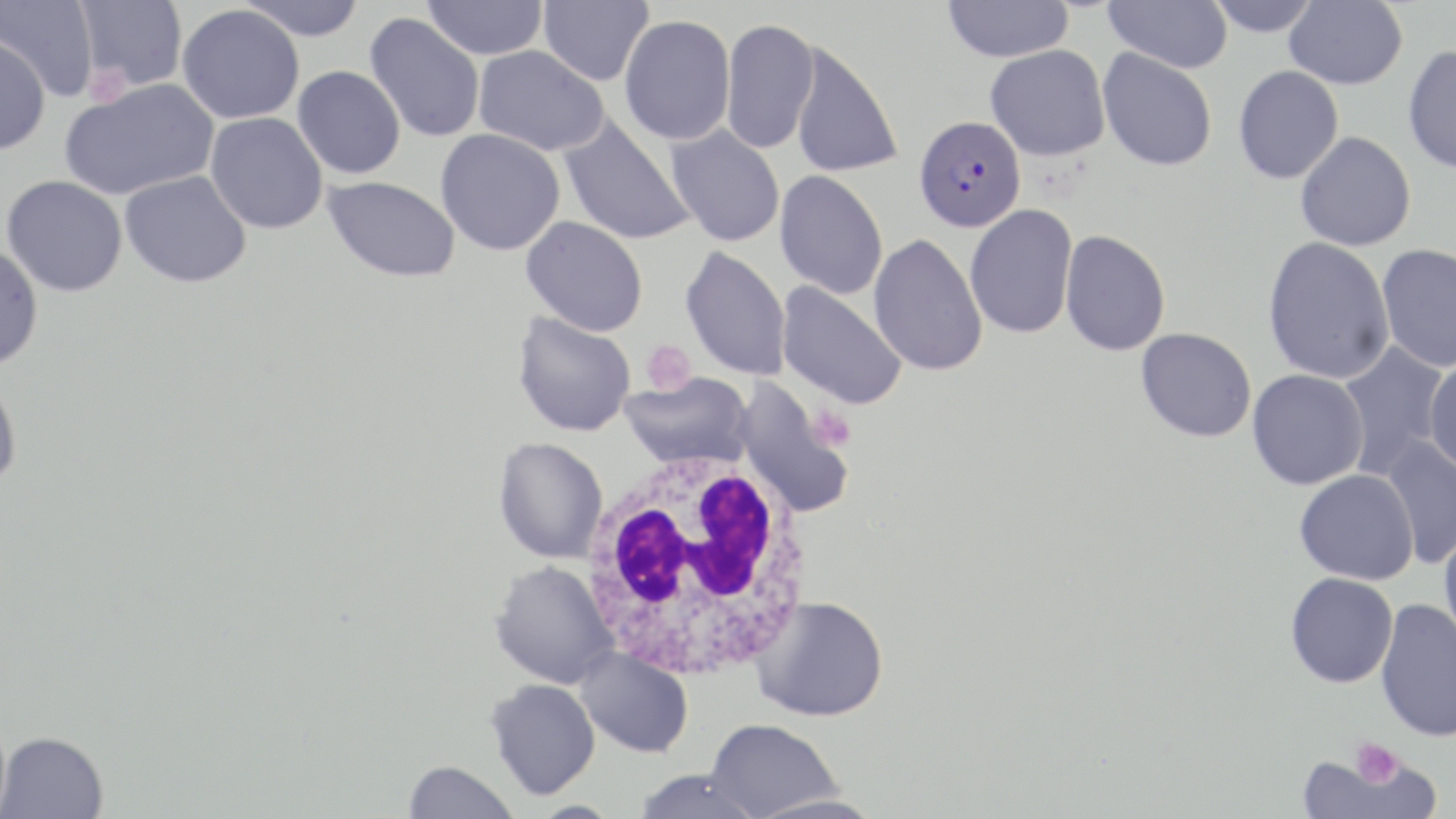

slide-level diagnosis = Plasmodium falciparum
preparation = thin blood film
magnification = 1000x
modality = light microscopy
platelet locations = approximate bounding boxes as (x1,y1)-(x2,y2) corner pairs in pixels: (82,67)-(130,108), (640,339)-(697,395), (808,404)-(855,451), (1349,737)-(1402,788)
uninfected red blood cell locations = approximate bounding boxes as (x1,y1)-(x2,y2) corner pairs in pixels: (0,0)-(100,102), (75,0)-(187,91), (235,0)-(367,41), (422,0)-(548,60), (538,0)-(653,86), (941,0)-(1074,63), (1104,0)-(1232,73), (1205,0)-(1322,37), (1284,1)-(1408,90), (177,5)-(304,124), (365,13)-(485,143), (619,15)-(736,145), (721,18)-(821,155), (0,35)-(50,156), (790,41)-(903,179), (1403,44)-(1456,174), (473,45)-(609,156), (985,45)-(1110,161), (1097,47)-(1218,171), (293,65)-(406,179), (1232,66)-(1343,185), (60,79)-(220,200), (557,112)-(697,247), (205,113)-(328,234), (665,123)-(786,248), (435,129)-(566,256), (1295,131)-(1416,251), (119,170)-(252,289), (775,170)-(888,300), (2,176)-(128,297), (322,176)-(461,283), (964,204)-(1078,339), (521,216)-(649,336), (1060,229)-(1170,357), (869,233)-(988,377), (1262,236)-(1396,385), (1376,243)-(1456,372), (0,244)-(44,370), (680,245)-(792,381), (776,281)-(908,410), (512,312)-(636,437), (1135,327)-(1257,443), (1336,341)-(1450,479), (1424,355)-(1456,479), (1247,369)-(1369,490), (621,372)-(754,471), (0,373)-(23,491), (734,379)-(855,517), (1380,435)-(1456,570), (492,436)-(608,564), (1294,469)-(1419,585), (1438,527)-(1456,647), (487,560)-(619,689), (1285,573)-(1398,688), (751,596)-(889,722), (1375,599)-(1456,743), (574,647)-(694,758), (485,679)-(601,801), (705,718)-(843,819), (0,731)-(108,819), (1298,750)-(1426,819), (402,760)-(519,819), (632,769)-(763,819), (748,792)-(883,819)
Plasmodium falciparum-infected red blood cell locations = approximate bounding boxes as (x1,y1)-(x2,y2) corner pairs in pixels: (914,115)-(1026,232)
image size = 1456×819 pixels
white blood cell locations = approximate bounding boxes as (x1,y1)-(x2,y2) corner pairs in pixels: (580,443)-(816,686)
field of view = one of a larger specimen
stain = May-Grünwald-Giemsa